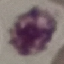
malaria_status: uninfected
capture: smartphone through the microscope eyepiece
image_type: automatically extracted cell patch, resized to 64 × 64 pixels
stain: Giemsa
preparation: thin blood smear